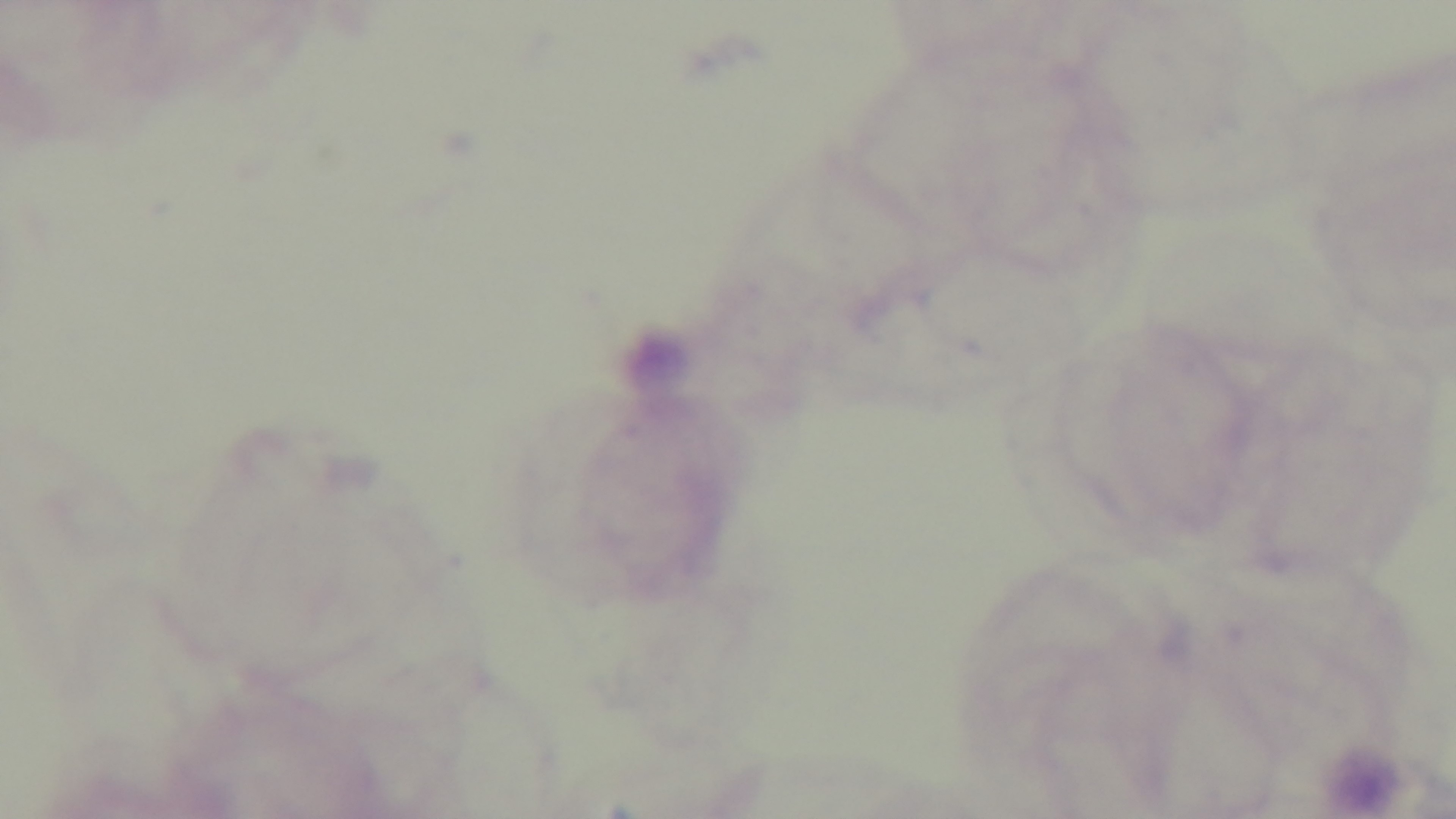

malaria status = uninfected
modality = light microscopy
field of view = single
objective = 100x oil immersion
stain = Giemsa
preparation = thick
capture = mounted 4K digital camera